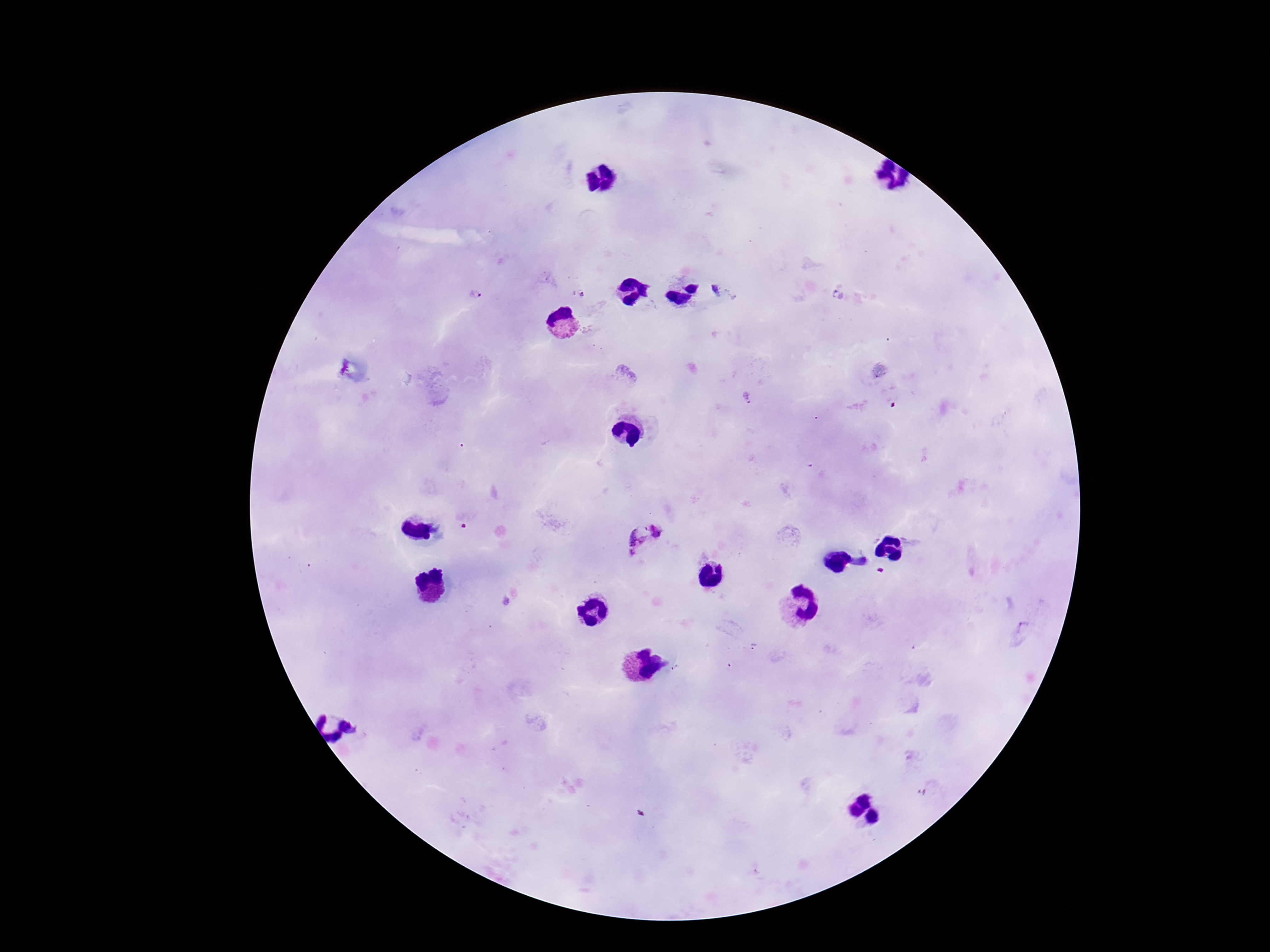
{
  "magnification": "100x",
  "stain": "Giemsa",
  "field_of_view": "single",
  "patient_malaria_status": "positive",
  "image_size": "1270×952 pixels",
  "preparation": "thick blood film",
  "capture": "smartphone camera through the microscope eyepiece",
  "plasmodium_parasite_locations": "approximate centers as [x, y] in pixels: [716, 289], [582, 293], [476, 294], [660, 530], [634, 533], [632, 554]"
}